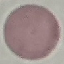
result = no malaria parasites detected
stain = Giemsa
preparation = thin smear
image type = cell patch, automatically extracted from a larger field of view and resized to 64 × 64 pixels
capture = smartphone through the microscope eyepiece